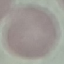

Summary:
  - Malaria status: uninfected
  - Image type: automatically extracted cell patch, resized to 64 × 64 pixels
  - Capture: smartphone camera at the microscope eyepiece
  - Stain: Giemsa
  - Preparation: thin blood film